Which red blood cells are P. falciparum-infected, and which are of indeterminate infection status?
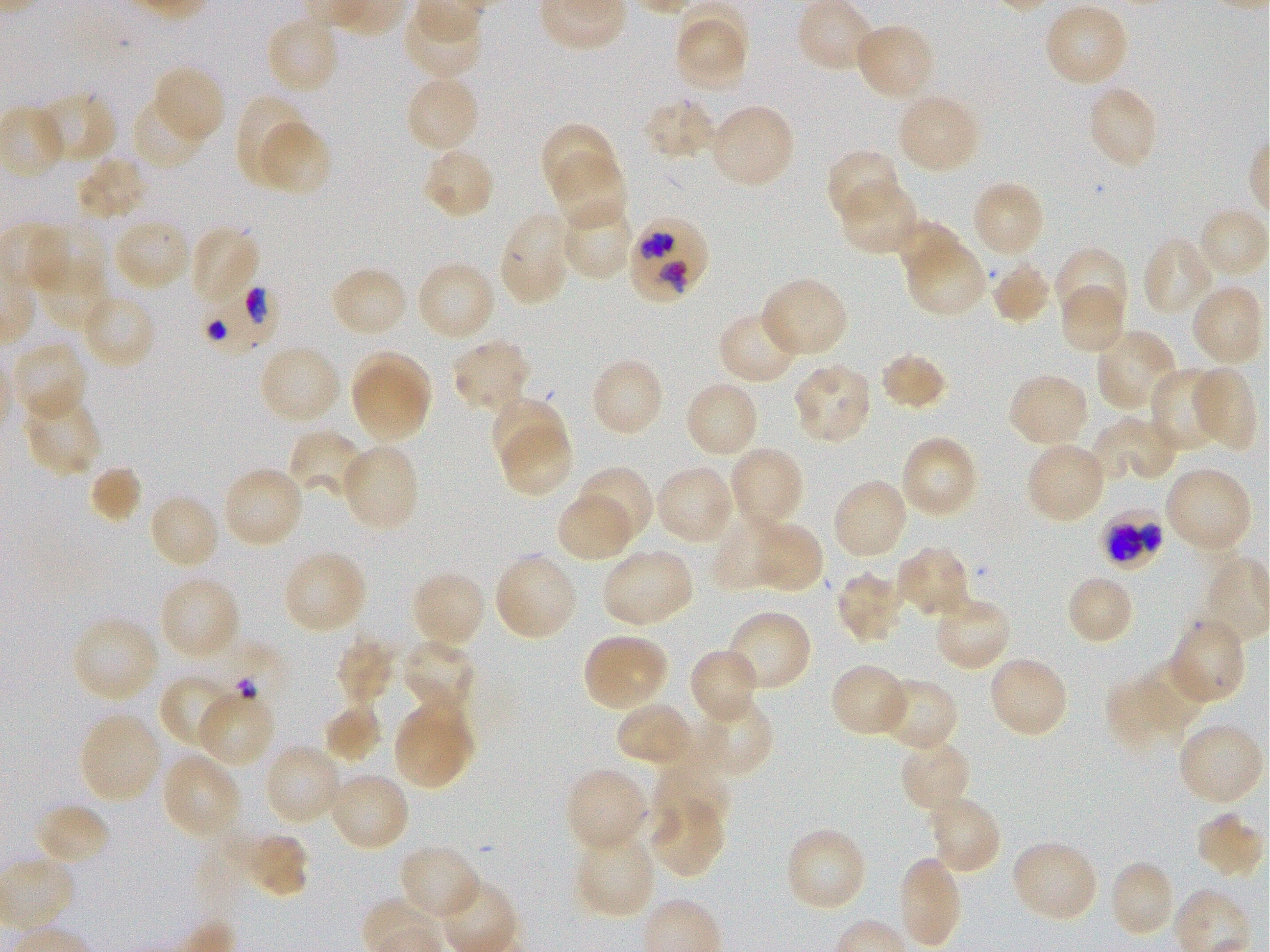

Approximate bounding boxes as {x1, y1, x2, y2} in pixels. Not every red blood cell is marked.
Infected red blood cells: {629, 217, 708, 302}, {201, 285, 279, 353}, {1101, 509, 1164, 570}.
Red blood cells of indeterminate infection status: {215, 639, 285, 707}.

{
  "locations_of_uninfected_red_blood_cells": "{1043, 3, 1129, 89}, {402, 7, 484, 80}, {265, 15, 341, 95}, {676, 16, 747, 90}, {853, 22, 935, 101}, {154, 67, 225, 143}, {405, 75, 480, 154}, {1086, 85, 1160, 170}, {37, 91, 118, 167}, {895, 93, 981, 174}, {236, 94, 308, 182}, {131, 96, 207, 170}, {641, 97, 717, 163}, {708, 103, 797, 189}, {0, 105, 66, 181}, {255, 119, 331, 195}, {538, 122, 618, 201}, {421, 146, 496, 221}, {825, 148, 902, 223}, {550, 155, 628, 232}, {74, 156, 148, 222}, {839, 180, 920, 256}, {970, 180, 1046, 259}, {560, 202, 635, 282}, {1197, 207, 1268, 281}, {498, 211, 573, 306}, {112, 217, 192, 292}, {895, 219, 966, 283}, {190, 225, 260, 305}, {31, 227, 107, 293}, {1141, 237, 1218, 317}, {905, 239, 986, 317}, {1055, 248, 1129, 323}, {35, 260, 111, 333}, {415, 260, 496, 342}, {991, 260, 1053, 326}, {328, 265, 409, 339}, {760, 276, 850, 358}, {1190, 284, 1265, 368}, {1058, 285, 1126, 355}, {81, 293, 157, 371}, {718, 308, 802, 384}, {1096, 328, 1177, 413}, {451, 337, 531, 416}, {11, 342, 87, 424}, {258, 344, 342, 425}, {878, 351, 950, 412}, {351, 354, 431, 440}, {588, 357, 665, 439}, {791, 364, 874, 444}, {1193, 365, 1257, 449}, {1148, 367, 1226, 454}, {1007, 373, 1090, 450}, {684, 381, 760, 459}, {22, 391, 103, 478}, {489, 395, 567, 470}, {1092, 417, 1176, 485}, {498, 423, 572, 497}, {291, 429, 366, 497}, {899, 435, 979, 520}, {1024, 441, 1107, 524}, {340, 442, 420, 532}, {729, 446, 806, 528}, {655, 464, 735, 545}, {221, 465, 305, 548}, {575, 465, 656, 544}, {89, 466, 142, 523}, {1164, 466, 1253, 554}, {831, 478, 909, 560}, {147, 493, 221, 571}, {555, 494, 634, 562}, {710, 514, 787, 592}, {751, 520, 825, 595}, {894, 544, 971, 620}, {601, 548, 696, 627}, {282, 550, 367, 634}, {493, 551, 579, 642}, {409, 570, 487, 649}, {834, 571, 905, 643}, {1065, 573, 1135, 646}, {158, 575, 242, 659}, {932, 593, 1012, 673}, {725, 610, 813, 693}, {71, 615, 160, 702}, {1169, 617, 1246, 705}, {581, 633, 670, 711}, {335, 637, 397, 707}, {398, 638, 477, 715}, {688, 647, 761, 726}, {986, 656, 1070, 739}, {1136, 660, 1206, 729}, {830, 664, 910, 738}, {159, 674, 237, 751}, {878, 677, 959, 753}, {1105, 678, 1176, 754}, {196, 690, 276, 767}, {692, 698, 775, 778}, {322, 699, 382, 763}, {615, 701, 695, 769}, {392, 703, 475, 789}, {78, 712, 162, 804}, {1181, 727, 1264, 802}, {898, 739, 972, 814}, {264, 743, 344, 826}, {161, 751, 242, 838}, {651, 760, 731, 834}, {564, 766, 649, 854}, {328, 771, 411, 852}, {647, 798, 725, 880}, {929, 798, 1001, 871}, {34, 803, 112, 866}, {1195, 811, 1264, 880}, {237, 832, 309, 899}, {791, 833, 864, 907}, {580, 838, 652, 914}, {398, 845, 481, 922}, {1014, 845, 1096, 918}, {901, 859, 959, 946}, {1114, 863, 1170, 934}",
  "objective": "100x, oil immersion, numerical aperture 1.25",
  "field_of_view": "single",
  "preparation": "thin blood smear",
  "image_size": "1270×952 pixels",
  "culture": "in-vitro P. falciparum strain 3D7, static",
  "stain": "Giemsa",
  "donor_blood_group": "O+"
}